Outline each uninfected red blood cell.
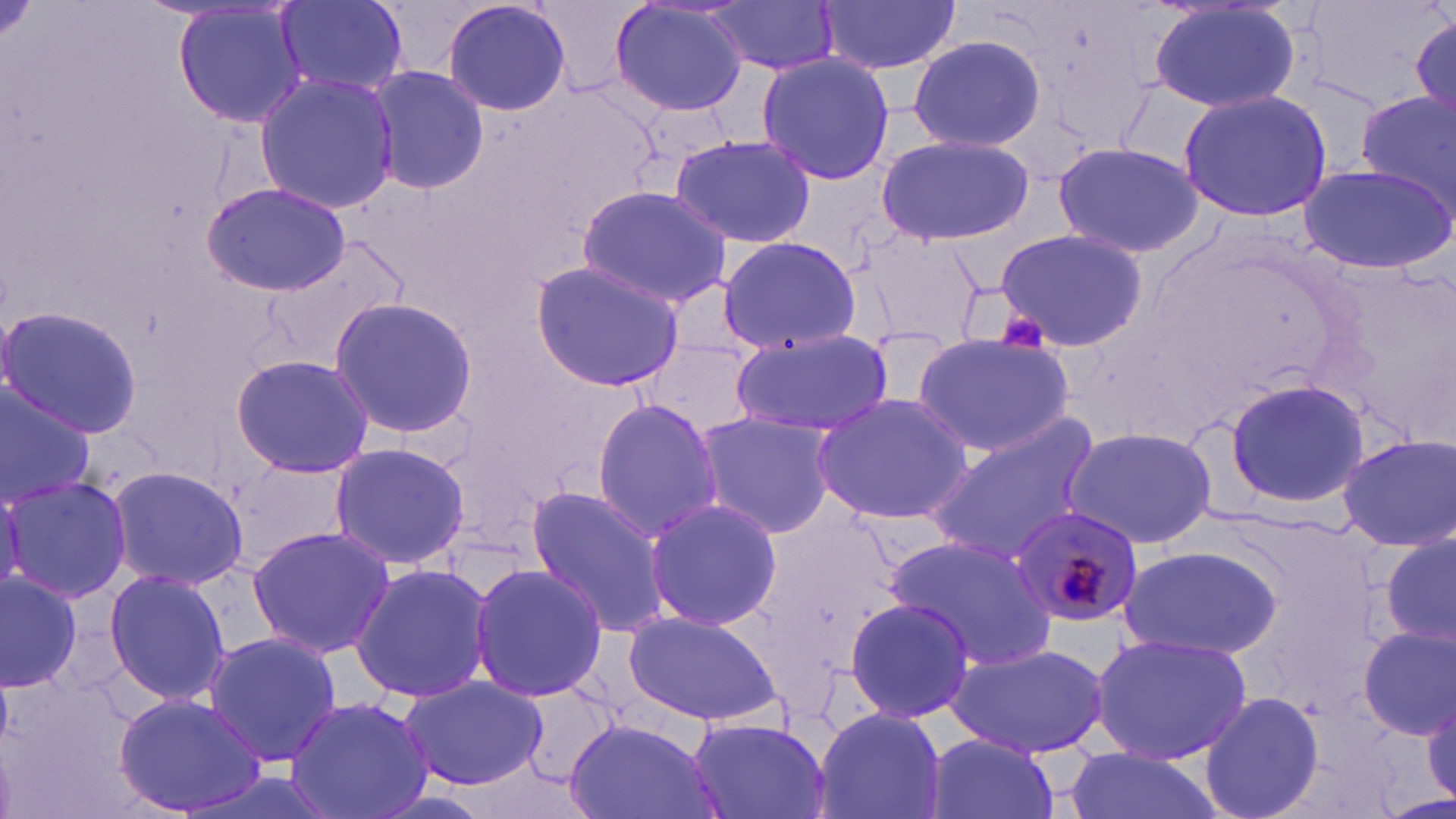
Approximate bounding boxes as named x1/y1/x2/y2 corners in pixels.
Uninfected red blood cells: (x1=441, y1=0, x2=573, y2=119), (x1=608, y1=0, x2=751, y2=118), (x1=274, y1=1, x2=407, y2=97), (x1=704, y1=1, x2=842, y2=74), (x1=816, y1=1, x2=961, y2=74), (x1=172, y1=2, x2=309, y2=129), (x1=1145, y1=2, x2=1306, y2=114), (x1=1409, y1=11, x2=1456, y2=127), (x1=906, y1=33, x2=1046, y2=154), (x1=756, y1=51, x2=894, y2=186), (x1=366, y1=63, x2=487, y2=196), (x1=254, y1=72, x2=401, y2=213), (x1=1177, y1=87, x2=1333, y2=222), (x1=1354, y1=89, x2=1456, y2=210), (x1=875, y1=134, x2=1036, y2=245), (x1=670, y1=135, x2=816, y2=246), (x1=1052, y1=140, x2=1206, y2=260), (x1=1298, y1=160, x2=1454, y2=275), (x1=201, y1=183, x2=350, y2=295), (x1=577, y1=186, x2=735, y2=309), (x1=994, y1=227, x2=1146, y2=352), (x1=262, y1=230, x2=408, y2=371), (x1=717, y1=234, x2=861, y2=354), (x1=863, y1=235, x2=985, y2=343), (x1=529, y1=260, x2=688, y2=392), (x1=328, y1=297, x2=480, y2=437), (x1=0, y1=305, x2=144, y2=437), (x1=730, y1=329, x2=894, y2=439), (x1=912, y1=333, x2=1075, y2=457), (x1=640, y1=338, x2=761, y2=437), (x1=229, y1=353, x2=375, y2=478), (x1=0, y1=375, x2=97, y2=506), (x1=1223, y1=376, x2=1369, y2=509), (x1=811, y1=393, x2=975, y2=525), (x1=591, y1=398, x2=725, y2=540), (x1=695, y1=410, x2=838, y2=537), (x1=925, y1=415, x2=1101, y2=566), (x1=1060, y1=424, x2=1219, y2=550), (x1=1335, y1=434, x2=1456, y2=552), (x1=328, y1=441, x2=470, y2=571), (x1=106, y1=463, x2=249, y2=590), (x1=1, y1=474, x2=132, y2=606), (x1=523, y1=487, x2=672, y2=640), (x1=642, y1=496, x2=783, y2=633), (x1=246, y1=525, x2=396, y2=659), (x1=1380, y1=532, x2=1456, y2=652), (x1=885, y1=537, x2=1059, y2=671), (x1=1118, y1=543, x2=1282, y2=661), (x1=350, y1=562, x2=492, y2=704), (x1=469, y1=562, x2=607, y2=703), (x1=102, y1=567, x2=230, y2=709), (x1=0, y1=572, x2=83, y2=694), (x1=841, y1=596, x2=976, y2=725), (x1=621, y1=610, x2=784, y2=727), (x1=1356, y1=625, x2=1456, y2=742), (x1=201, y1=632, x2=341, y2=764), (x1=1090, y1=632, x2=1253, y2=763), (x1=947, y1=642, x2=1111, y2=757), (x1=397, y1=674, x2=548, y2=789), (x1=1200, y1=690, x2=1324, y2=819), (x1=113, y1=693, x2=267, y2=815), (x1=285, y1=695, x2=436, y2=819), (x1=811, y1=708, x2=947, y2=819), (x1=685, y1=714, x2=830, y2=819), (x1=564, y1=717, x2=721, y2=819), (x1=922, y1=733, x2=1060, y2=819), (x1=1061, y1=747, x2=1220, y2=819).

Plasmodium malariae-infected red blood cell locations: (x1=1009, y1=505, x2=1143, y2=629). Platelet locations: (x1=1002, y1=315, x2=1054, y2=350). Slide-level diagnosis: Plasmodium malariae. Optical microscopy. Thin blood smear. May-Grünwald-Giemsa-stained preparation. 1000x magnification. Image is 1456×819 pixels. Single field of view.